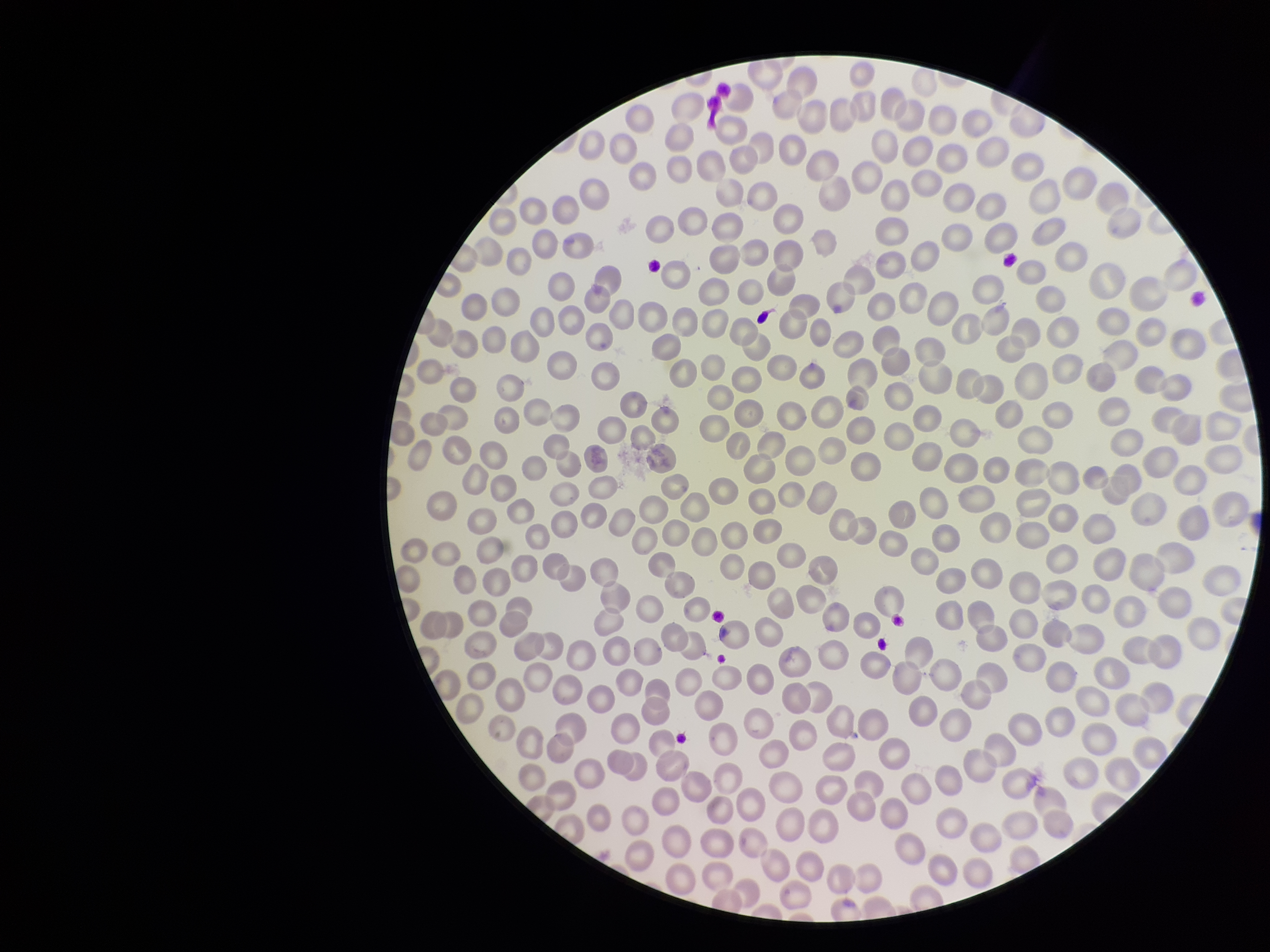
{
  "species_reported_for_this_patient": "Plasmodium falciparum",
  "parasitized_red_blood_cell_count": 0,
  "patient_malaria_status": "positive",
  "image_size": "1270×952 pixels",
  "stain": "Giemsa",
  "capture": "smartphone photograph through the microscope eyepiece",
  "preparation": "thin",
  "red_blood_cell_count": 348,
  "field_of_view": "one from this slide",
  "parasitized_red_blood_cells": "none seen"
}